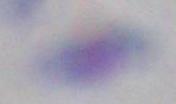

Summary:
  - Magnification: 1000x
  - Identification: Toxoplasma gondii
  - Modality: photomicrograph